Name the cell type shown.
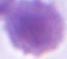
An erythrocyte.

1000x magnification. Micrograph.